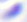

Summary:
  - Magnification: 400x
  - Identification: Toxoplasma gondii
  - Modality: photomicrograph